Report the malaria status.
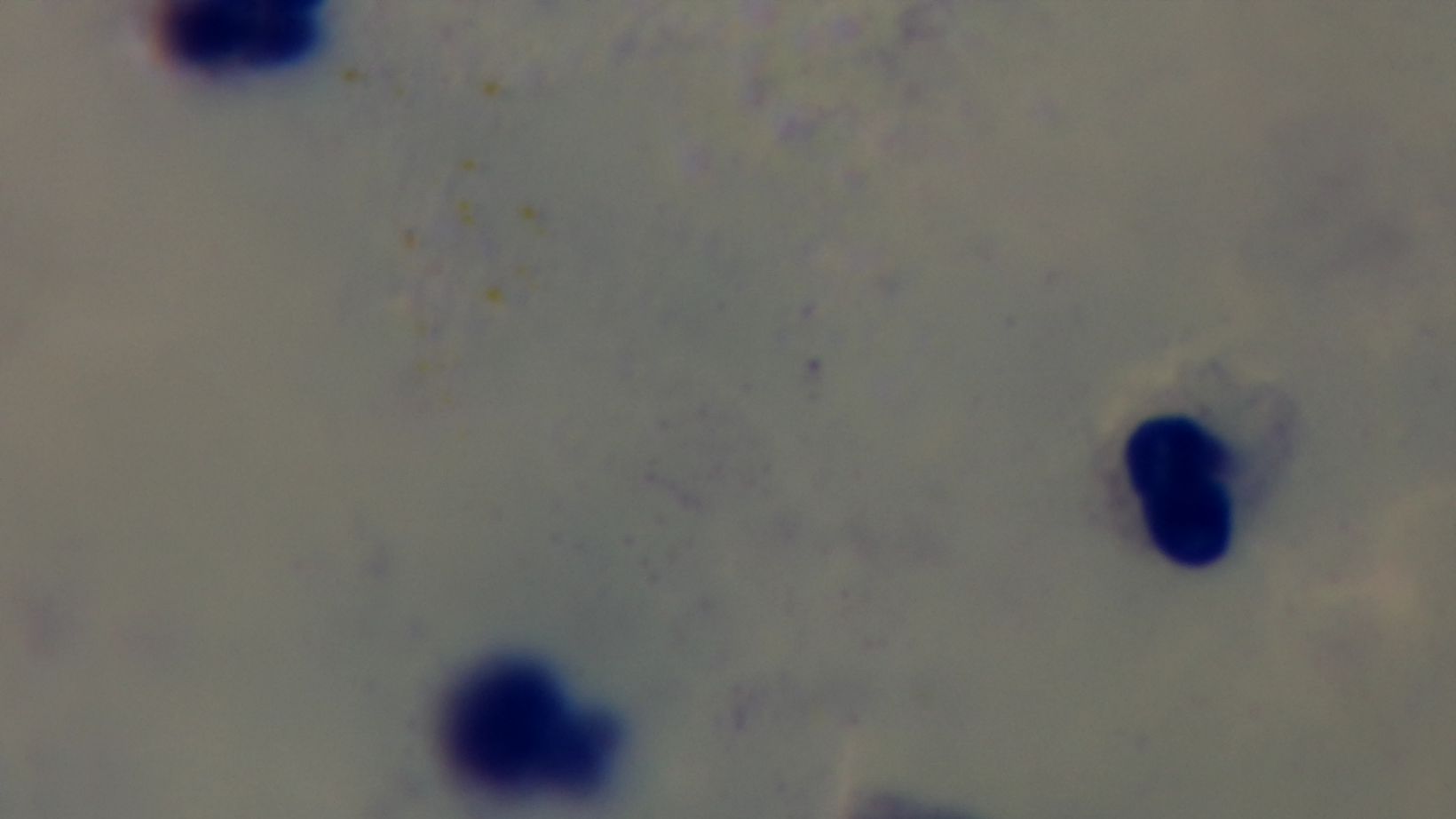

Uninfected.

Light microscopy. Preparation: thick. Giemsa-stained. One field from the slide. Mounted 4K digital camera. Oil-immersion objective, 100x.